Describe the morphology of the red blood cells.
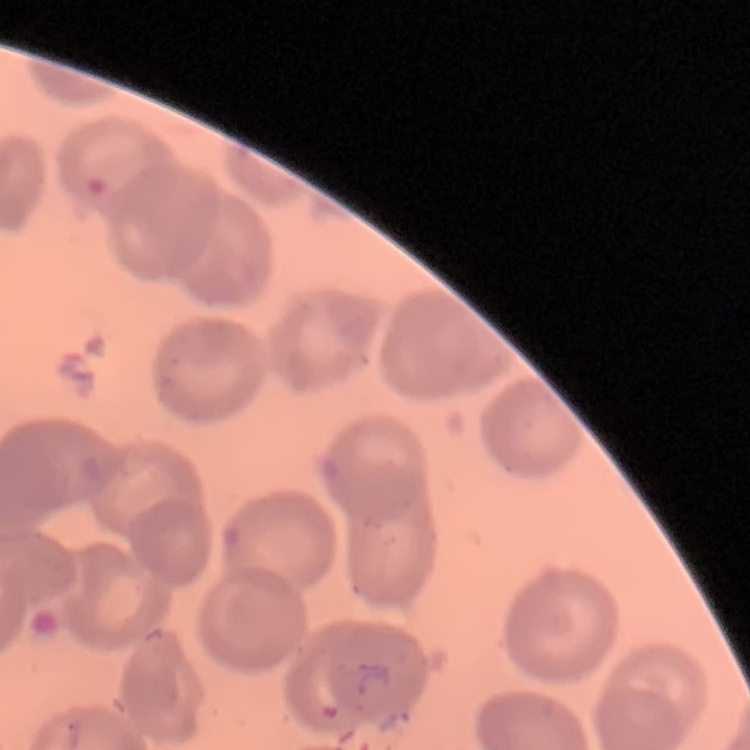
They show no rouleaux formation.

preparation = thin peripheral smear
image type = square crop of a larger photomicrograph
stain = Field's or Giemsa